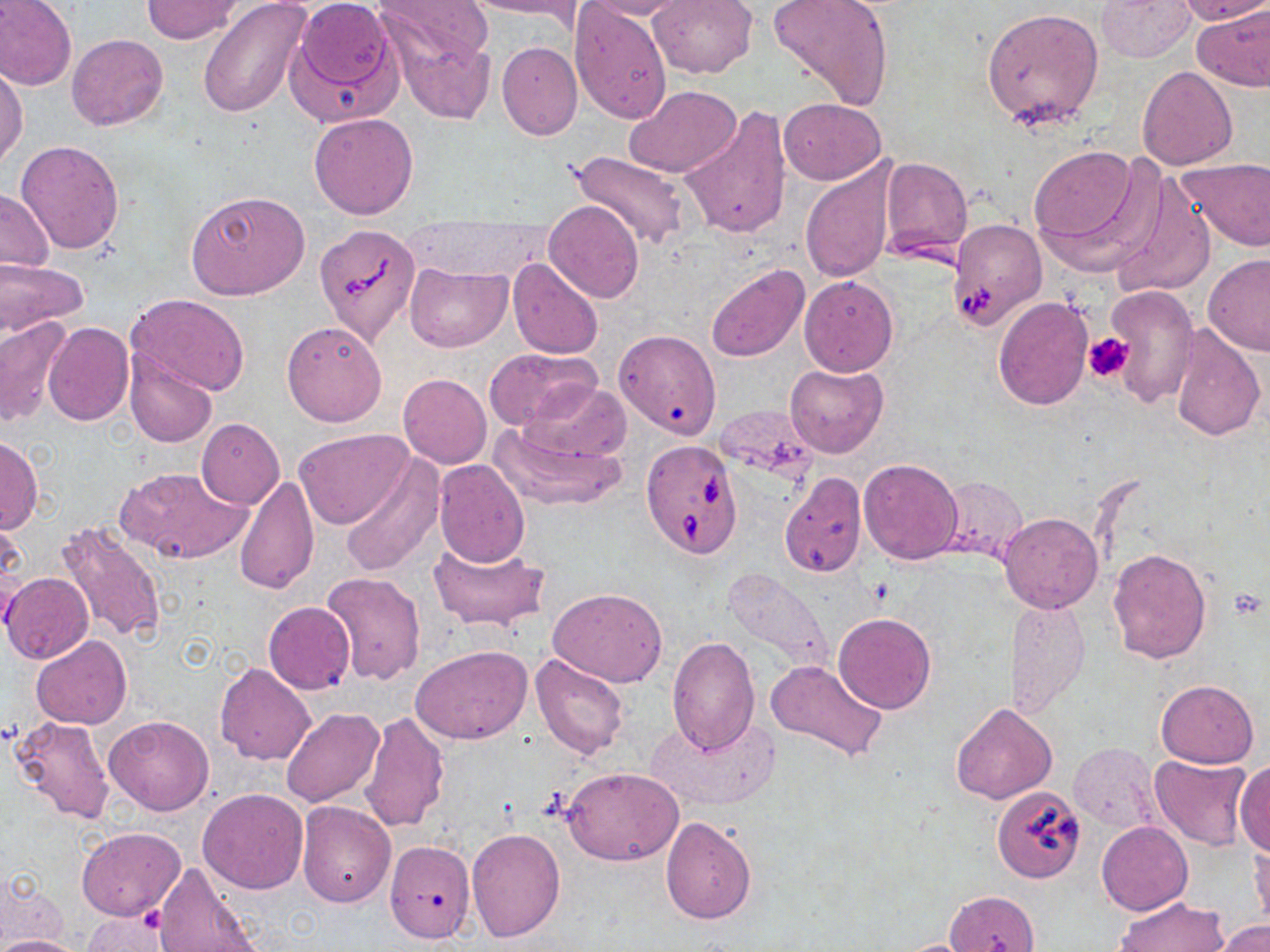
Approximate bounding boxes as (x1, y1, x2, y2) in pixels. Babesia divergens-infected red blood cell locations: (946, 218, 1048, 332), (316, 222, 420, 344), (641, 439, 742, 557), (991, 787, 1086, 884). Platelet locations: (1084, 332, 1133, 385). Uninfected red blood cell locations: (0, 0, 78, 91), (197, 0, 313, 117), (292, 0, 398, 108), (377, 0, 495, 71), (457, 0, 588, 20), (579, 0, 688, 22), (648, 0, 757, 78), (766, 0, 896, 111), (1094, 0, 1196, 62), (141, 1, 244, 43), (1172, 1, 1270, 25), (1192, 2, 1270, 91), (569, 3, 673, 125), (980, 8, 1105, 130), (393, 29, 495, 124), (68, 34, 168, 131), (496, 42, 583, 141), (1, 64, 28, 169), (1137, 66, 1237, 170), (625, 85, 741, 177), (778, 98, 885, 184), (680, 105, 792, 241), (308, 111, 420, 220), (16, 139, 126, 255), (1028, 145, 1154, 265), (561, 148, 691, 253), (879, 156, 972, 259), (1177, 158, 1270, 251), (800, 160, 898, 283), (1106, 173, 1216, 300), (0, 190, 55, 272), (184, 190, 311, 299), (545, 202, 644, 303), (1201, 252, 1270, 356), (507, 257, 605, 360), (0, 259, 88, 335), (405, 262, 509, 352), (706, 264, 809, 362), (798, 275, 899, 377), (1105, 285, 1197, 408), (125, 293, 252, 396), (993, 296, 1093, 410), (0, 316, 72, 429), (281, 320, 388, 427), (43, 321, 134, 426), (1166, 323, 1266, 443), (615, 329, 721, 438), (484, 347, 602, 433), (124, 350, 217, 448), (784, 363, 887, 458), (398, 374, 491, 468), (524, 382, 631, 464), (713, 404, 818, 484), (196, 418, 285, 508), (490, 419, 627, 511), (210, 426, 298, 569), (296, 429, 414, 530), (1, 435, 42, 536), (338, 454, 442, 576), (859, 458, 963, 565), (433, 459, 529, 567), (118, 465, 251, 566), (779, 472, 868, 579), (233, 474, 320, 596), (935, 477, 1028, 563), (999, 513, 1102, 613), (0, 517, 25, 614), (55, 519, 168, 643), (429, 538, 548, 634), (1107, 548, 1212, 663), (722, 565, 836, 674), (321, 572, 426, 684), (3, 573, 93, 663), (548, 586, 669, 688), (1005, 597, 1090, 718), (262, 601, 356, 694), (833, 613, 936, 713), (31, 635, 132, 730), (667, 637, 760, 755), (411, 645, 531, 745), (531, 652, 629, 760), (766, 658, 887, 764), (214, 662, 316, 765), (1155, 680, 1259, 768), (950, 701, 1058, 804), (280, 708, 384, 808), (358, 712, 450, 832), (647, 712, 780, 812), (104, 715, 215, 816), (7, 716, 113, 826), (1070, 742, 1163, 834), (1149, 754, 1253, 851), (1233, 760, 1270, 857), (563, 768, 685, 866), (198, 788, 308, 894), (295, 801, 396, 907), (660, 816, 757, 923), (1097, 822, 1192, 914), (76, 826, 186, 921), (466, 828, 565, 941), (1249, 836, 1269, 933), (385, 839, 476, 943), (153, 862, 264, 952), (3, 876, 72, 949), (946, 890, 1041, 952), (1114, 896, 1227, 951), (84, 910, 174, 952), (1211, 920, 1270, 952), (2, 935, 87, 952), (890, 938, 985, 952). Slide-level diagnosis: Babesia divergens. May-Grünwald-Giemsa stain. Captured at 1000x magnification. Optical microscopy. Single field of view. Image is 1270×952 pixels. Thin blood film.